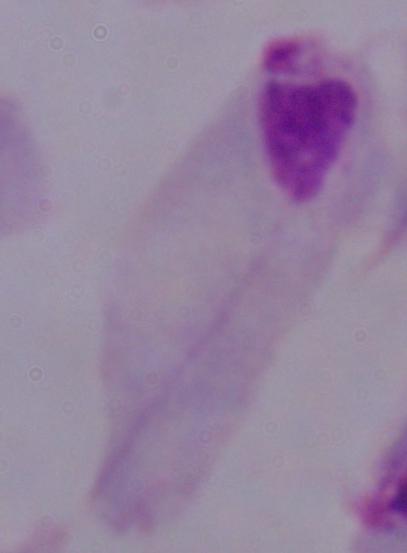

{
  "modality": "micrograph",
  "magnification": "1000x",
  "identification": "trichomonad"
}